Assess this cell for malaria.
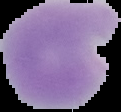
Parasitized.

preparation = thin blood film
image type = cell region segmented out of the field of view; surrounding area masked to black
image size = 121×112 pixels